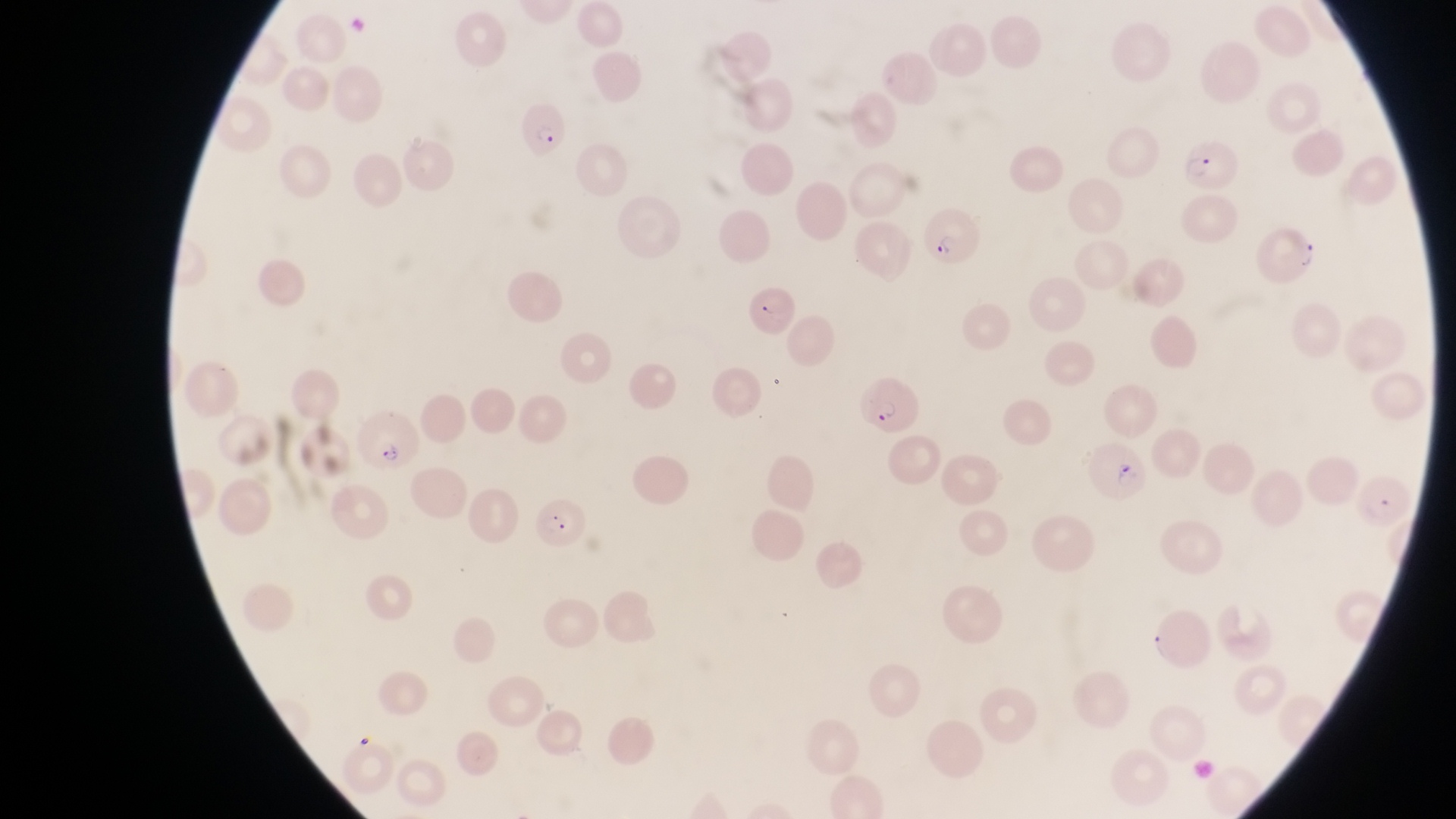

Approximate bounding boxes as left top right bottom in pixels.
Summary:
  - Parasitised red blood cell locations: 518 106 574 164; 1186 136 1247 194; 914 202 983 274; 1254 221 1320 292; 739 285 810 341; 851 367 920 431; 360 406 421 477; 1086 444 1153 503; 529 499 588 549
  - Country: Uganda
  - Field of view: single
  - Image size: 1456×819 pixels
  - Preparation: thin blood smear
  - Capture: smartphone photograph through the eyepiece of an Olympus CX-23 microscope
  - Magnification: 1000x